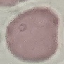

Malaria status: uninfected. Photographed with a smartphone camera at the microscope eyepiece. Thin blood film. Giemsa-stained preparation. Automatically extracted cell patch, resized to 64 × 64 pixels.